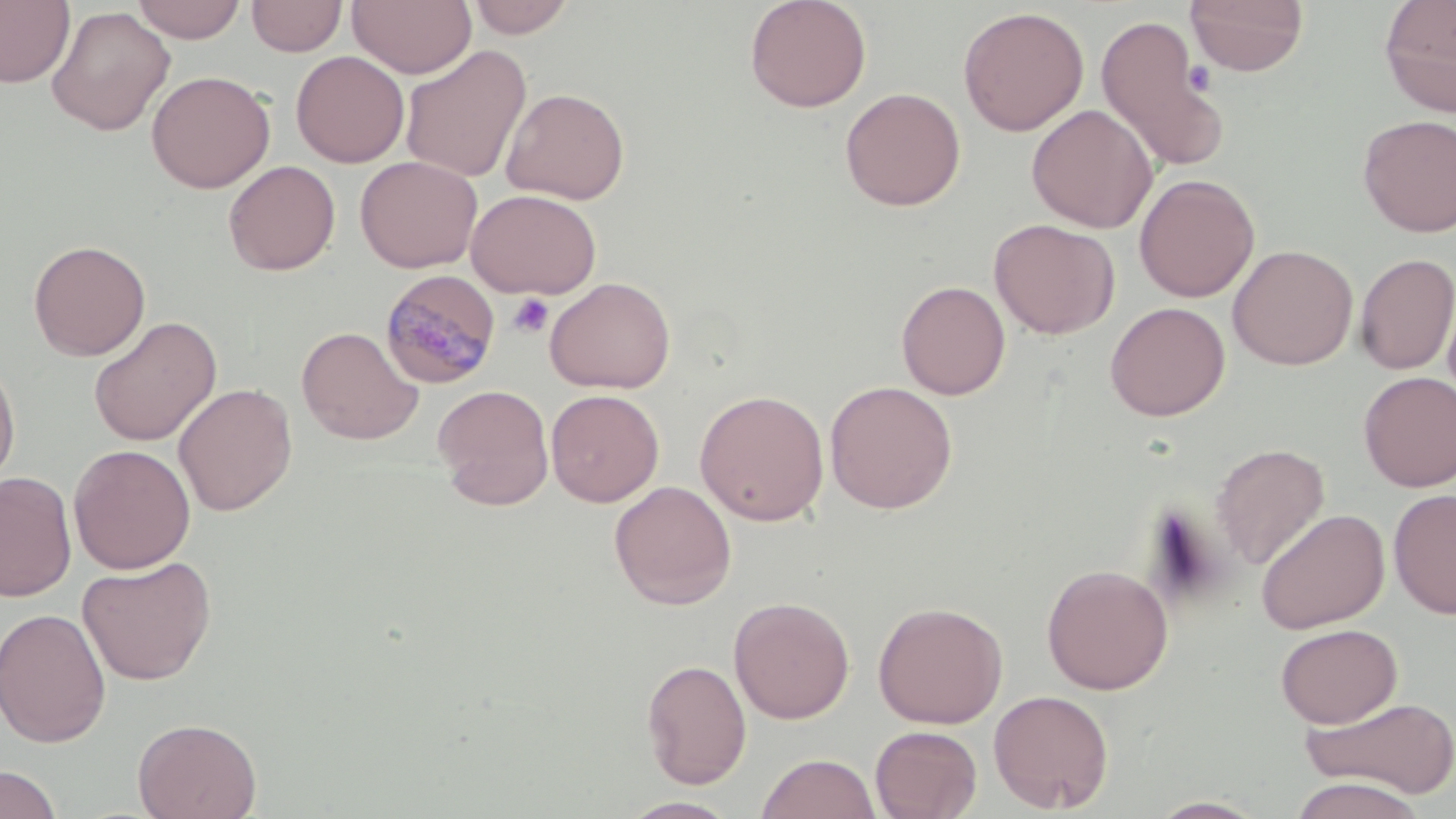
Summary:
  - Coordinate format: approximate bounding boxes as [x1, y1, x2, y2] in pixels
  - Plasmodium malariae-infected red blood cell locations: [380, 269, 502, 389]
  - Uninfected red blood cell locations: [0, 0, 76, 88], [130, 0, 246, 43], [465, 0, 579, 38], [743, 0, 872, 113], [1184, 0, 1310, 77], [1379, 0, 1456, 117], [247, 1, 347, 57], [347, 1, 477, 78], [46, 6, 175, 136], [957, 6, 1089, 136], [1095, 12, 1229, 174], [399, 45, 532, 183], [291, 50, 410, 168], [146, 69, 275, 193], [501, 87, 630, 205], [840, 87, 966, 211], [1027, 104, 1158, 233], [1356, 114, 1456, 237], [355, 155, 482, 273], [223, 160, 341, 275], [1134, 173, 1259, 302], [466, 188, 602, 299], [988, 218, 1120, 339], [28, 239, 151, 361], [1228, 244, 1358, 371], [1354, 252, 1456, 375], [544, 276, 676, 394], [895, 280, 1011, 400], [1104, 301, 1230, 421], [88, 316, 222, 447], [296, 326, 424, 445], [0, 351, 21, 492], [1358, 371, 1456, 491], [824, 380, 958, 514], [173, 382, 297, 516], [432, 384, 554, 510], [546, 389, 664, 507], [694, 389, 830, 526], [68, 443, 196, 574], [1211, 443, 1330, 570], [0, 470, 77, 602], [609, 480, 737, 610], [1388, 489, 1456, 619], [1256, 507, 1390, 634], [76, 556, 217, 686], [1041, 563, 1174, 695], [729, 596, 855, 724], [872, 600, 1008, 729], [0, 608, 111, 748], [1275, 623, 1402, 728], [641, 658, 752, 789], [988, 689, 1114, 814], [1300, 696, 1456, 799], [132, 716, 262, 819], [870, 725, 982, 819], [757, 752, 880, 819], [0, 764, 63, 819], [1289, 777, 1425, 819], [619, 796, 743, 818], [1148, 796, 1269, 818]
  - Platelet locations: [508, 293, 554, 338]
  - Slide-level diagnosis: Plasmodium malariae
  - Modality: optical microscopy
  - Preparation: thin blood film
  - Stain: May-Grünwald-Giemsa
  - Image size: 1456×819 pixels
  - Magnification: 1000x
  - Field of view: single